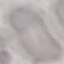 Result: no malaria parasites detected. Cell patch, automatically extracted from a larger field of view and resized to 64 × 64 pixels. Thin smear of blood. Giemsa stain. Acquired by smartphone through the microscope eyepiece.